State the blood parasite species.
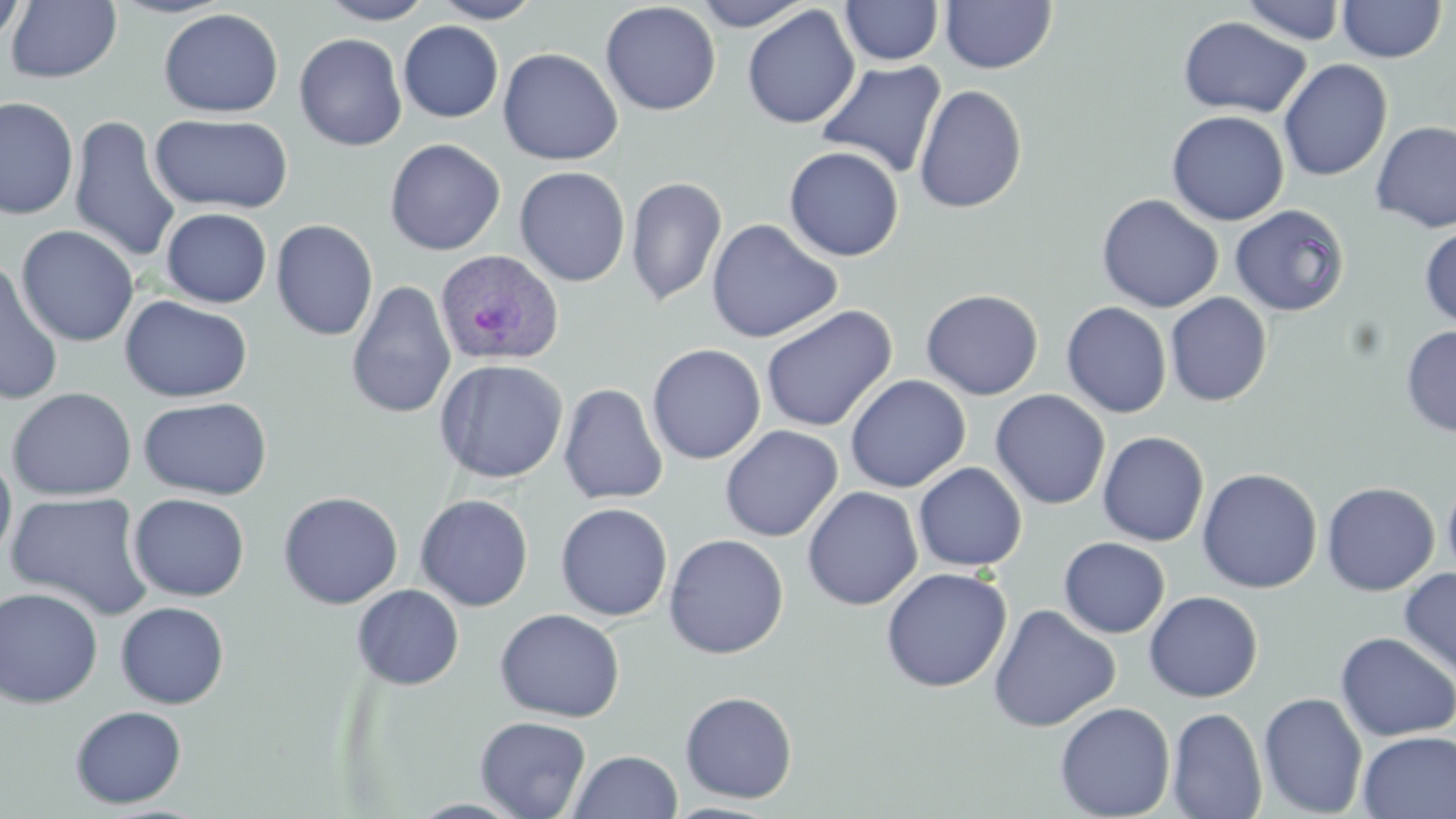
Plasmodium ovale.

Approximate bounding boxes as named x1/y1/x2/y2 corners in pixels. Uninfected red blood cell locations: (x1=107, y1=0, x2=237, y2=19), (x1=318, y1=0, x2=436, y2=25), (x1=432, y1=0, x2=543, y2=24), (x1=695, y1=0, x2=813, y2=31), (x1=1240, y1=0, x2=1347, y2=45), (x1=1337, y1=0, x2=1446, y2=63), (x1=0, y1=1, x2=29, y2=49), (x1=6, y1=1, x2=122, y2=83), (x1=840, y1=1, x2=944, y2=66), (x1=940, y1=1, x2=1057, y2=74), (x1=600, y1=2, x2=722, y2=116), (x1=742, y1=5, x2=860, y2=129), (x1=159, y1=8, x2=284, y2=117), (x1=1178, y1=16, x2=1312, y2=119), (x1=398, y1=21, x2=504, y2=123), (x1=294, y1=33, x2=407, y2=151), (x1=497, y1=47, x2=623, y2=165), (x1=1278, y1=58, x2=1393, y2=182), (x1=816, y1=60, x2=947, y2=178), (x1=913, y1=84, x2=1027, y2=214), (x1=0, y1=96, x2=79, y2=220), (x1=1166, y1=110, x2=1290, y2=226), (x1=150, y1=113, x2=294, y2=214), (x1=69, y1=115, x2=181, y2=265), (x1=1370, y1=120, x2=1456, y2=232), (x1=384, y1=138, x2=506, y2=256), (x1=784, y1=146, x2=905, y2=262), (x1=514, y1=166, x2=631, y2=287), (x1=625, y1=175, x2=728, y2=307), (x1=1096, y1=193, x2=1224, y2=313), (x1=1230, y1=204, x2=1350, y2=316), (x1=146, y1=206, x2=264, y2=403), (x1=160, y1=207, x2=272, y2=307), (x1=706, y1=218, x2=842, y2=343), (x1=270, y1=219, x2=379, y2=341), (x1=16, y1=225, x2=140, y2=347), (x1=1419, y1=227, x2=1456, y2=328), (x1=0, y1=259, x2=64, y2=406), (x1=346, y1=281, x2=456, y2=420), (x1=921, y1=289, x2=1043, y2=400), (x1=1165, y1=292, x2=1273, y2=407), (x1=119, y1=295, x2=253, y2=403), (x1=1061, y1=301, x2=1172, y2=418), (x1=761, y1=305, x2=898, y2=433), (x1=1400, y1=325, x2=1456, y2=437), (x1=646, y1=344, x2=766, y2=464), (x1=433, y1=358, x2=568, y2=484), (x1=845, y1=374, x2=970, y2=493), (x1=558, y1=383, x2=669, y2=505), (x1=7, y1=387, x2=137, y2=501), (x1=990, y1=389, x2=1111, y2=510), (x1=139, y1=396, x2=272, y2=500), (x1=720, y1=425, x2=843, y2=542), (x1=1097, y1=431, x2=1209, y2=546), (x1=0, y1=449, x2=17, y2=563), (x1=913, y1=462, x2=1027, y2=572), (x1=1196, y1=467, x2=1322, y2=593), (x1=1442, y1=474, x2=1456, y2=587), (x1=1321, y1=481, x2=1440, y2=595), (x1=802, y1=486, x2=923, y2=611), (x1=6, y1=491, x2=155, y2=621), (x1=278, y1=491, x2=404, y2=609), (x1=128, y1=493, x2=250, y2=601), (x1=415, y1=494, x2=534, y2=612), (x1=555, y1=502, x2=673, y2=621), (x1=664, y1=533, x2=789, y2=659), (x1=1059, y1=537, x2=1170, y2=637), (x1=881, y1=567, x2=1012, y2=692), (x1=1398, y1=567, x2=1456, y2=683), (x1=351, y1=584, x2=465, y2=690), (x1=0, y1=586, x2=104, y2=709), (x1=1143, y1=590, x2=1263, y2=702), (x1=115, y1=601, x2=229, y2=708), (x1=987, y1=603, x2=1121, y2=732), (x1=495, y1=608, x2=626, y2=722), (x1=1335, y1=631, x2=1456, y2=742), (x1=680, y1=691, x2=798, y2=803), (x1=1258, y1=692, x2=1368, y2=817), (x1=1054, y1=701, x2=1176, y2=819), (x1=69, y1=705, x2=187, y2=809), (x1=1167, y1=707, x2=1268, y2=819), (x1=475, y1=716, x2=592, y2=818), (x1=1357, y1=731, x2=1455, y2=818), (x1=567, y1=750, x2=683, y2=818), (x1=661, y1=801, x2=784, y2=818). Plasmodium ovale-infected red blood cell locations: (x1=434, y1=248, x2=565, y2=366). Single field of view. 1000x magnification. Image is 1456×819 pixels. Thin blood smear. Optical microscopy. May-Grünwald-Giemsa stain.